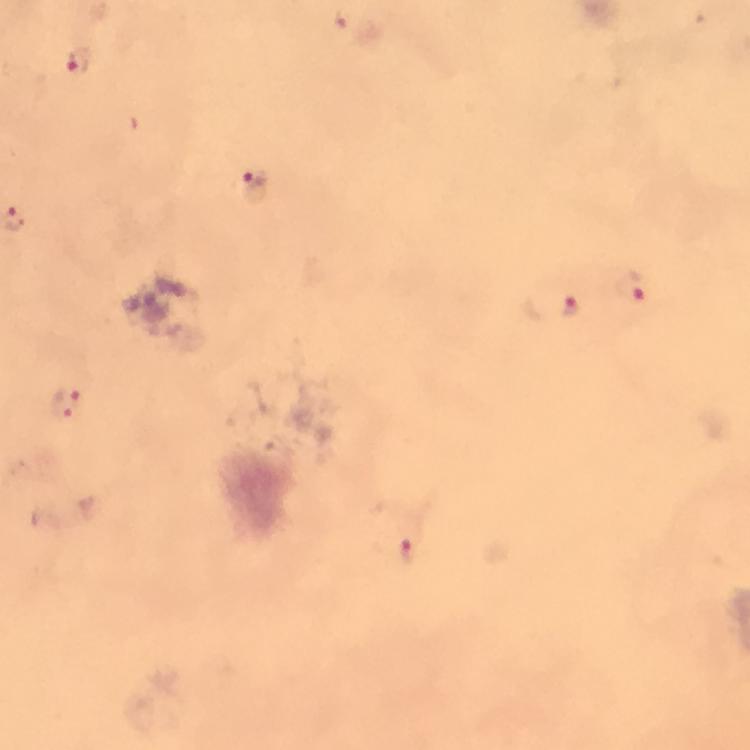
Approximate centers as [x, y] in pixels.
Summary:
  - Malaria parasite locations: [77, 60], [254, 182], [632, 285], [570, 308], [66, 404], [407, 550]
  - Cropped from: one field of view
  - Capture: smartphone camera through the microscope
  - Magnification: 100x
  - Immersion oil: used
  - Preparation: thick smear
  - Stain: Giemsa
  - Context: from a malaria diagnostic workup
  - Image size: 750×750 pixels